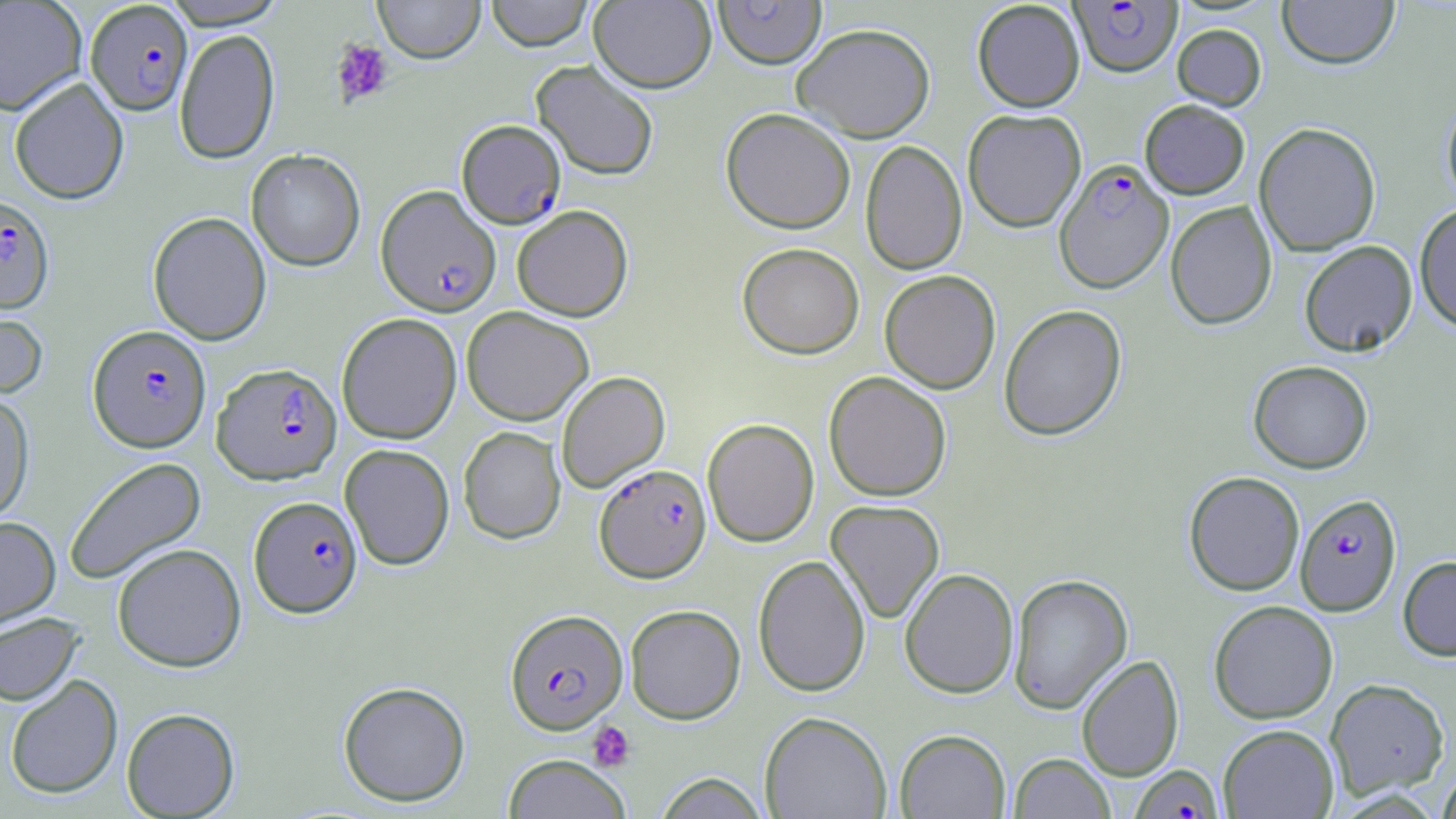

Summary:
  - Coordinate format: approximate bounding boxes as named x1/y1/x2/y2 corners in pixels
  - Plasmodium falciparum-infected red blood cell locations (subset): (x1=85, y1=1, x2=193, y2=115), (x1=457, y1=119, x2=566, y2=229), (x1=1054, y1=158, x2=1174, y2=293), (x1=376, y1=185, x2=502, y2=316), (x1=0, y1=194, x2=54, y2=313), (x1=88, y1=324, x2=211, y2=452), (x1=212, y1=363, x2=342, y2=484), (x1=595, y1=463, x2=711, y2=582), (x1=1295, y1=492, x2=1403, y2=615), (x1=249, y1=495, x2=363, y2=618), (x1=505, y1=608, x2=627, y2=734)
  - Uninfected red blood cell locations (subset): (x1=0, y1=0, x2=87, y2=114), (x1=374, y1=0, x2=485, y2=63), (x1=484, y1=0, x2=594, y2=51), (x1=1277, y1=0, x2=1400, y2=69), (x1=159, y1=1, x2=289, y2=29), (x1=589, y1=1, x2=716, y2=93), (x1=713, y1=1, x2=826, y2=68), (x1=972, y1=1, x2=1085, y2=112), (x1=793, y1=22, x2=935, y2=142), (x1=1172, y1=23, x2=1266, y2=110), (x1=175, y1=29, x2=281, y2=163), (x1=531, y1=60, x2=659, y2=180), (x1=8, y1=77, x2=129, y2=204), (x1=1441, y1=93, x2=1456, y2=212), (x1=1139, y1=99, x2=1250, y2=199), (x1=720, y1=107, x2=855, y2=233), (x1=962, y1=108, x2=1087, y2=233), (x1=1254, y1=122, x2=1381, y2=256), (x1=860, y1=140, x2=967, y2=275), (x1=246, y1=149, x2=365, y2=271), (x1=1165, y1=201, x2=1277, y2=331), (x1=1414, y1=202, x2=1456, y2=333), (x1=511, y1=204, x2=633, y2=322), (x1=148, y1=212, x2=272, y2=345), (x1=1299, y1=240, x2=1418, y2=357), (x1=737, y1=242, x2=864, y2=359), (x1=880, y1=270, x2=1001, y2=394), (x1=999, y1=304, x2=1127, y2=441), (x1=0, y1=306, x2=49, y2=402), (x1=461, y1=306, x2=594, y2=426), (x1=336, y1=313, x2=462, y2=444), (x1=1248, y1=360, x2=1373, y2=474), (x1=556, y1=371, x2=670, y2=492), (x1=824, y1=371, x2=951, y2=501), (x1=0, y1=392, x2=35, y2=525), (x1=702, y1=418, x2=820, y2=547), (x1=458, y1=426, x2=566, y2=544), (x1=339, y1=444, x2=455, y2=570), (x1=63, y1=456, x2=206, y2=584), (x1=1183, y1=471, x2=1305, y2=596), (x1=825, y1=500, x2=945, y2=622), (x1=0, y1=516, x2=60, y2=629), (x1=112, y1=543, x2=246, y2=671), (x1=753, y1=554, x2=871, y2=697), (x1=1398, y1=556, x2=1456, y2=660), (x1=900, y1=567, x2=1019, y2=698), (x1=1008, y1=573, x2=1132, y2=713), (x1=1208, y1=600, x2=1338, y2=724), (x1=625, y1=604, x2=746, y2=724), (x1=0, y1=612, x2=84, y2=706), (x1=1076, y1=654, x2=1184, y2=782), (x1=5, y1=674, x2=123, y2=799), (x1=1325, y1=678, x2=1450, y2=800), (x1=338, y1=680, x2=470, y2=807), (x1=121, y1=707, x2=240, y2=818), (x1=759, y1=711, x2=892, y2=819), (x1=1218, y1=724, x2=1339, y2=818), (x1=894, y1=728, x2=1010, y2=819), (x1=1009, y1=753, x2=1115, y2=818), (x1=502, y1=754, x2=631, y2=819), (x1=1435, y1=766, x2=1456, y2=818), (x1=653, y1=773, x2=769, y2=818)
  - Platelet locations: (x1=332, y1=39, x2=394, y2=108), (x1=587, y1=721, x2=635, y2=771)
  - Slide-level diagnosis: Plasmodium falciparum
  - Stain: May-Grünwald-Giemsa
  - Field of view: single
  - Modality: light microscopy
  - Preparation: thin blood film
  - Magnification: 1000x
  - Image size: 1456×819 pixels